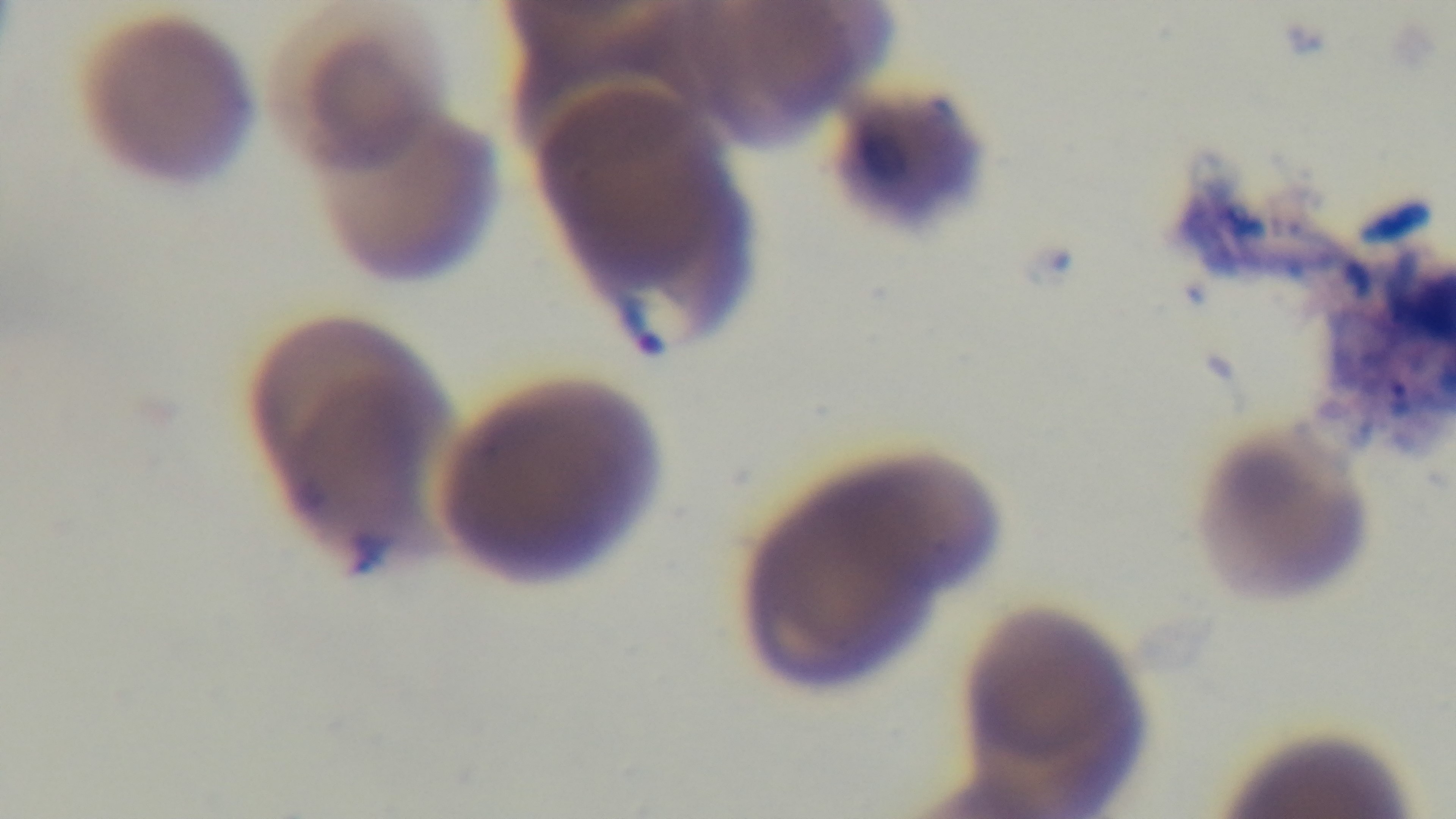

stain: Giemsa
field_of_view: one from the slide
modality: light microscopy
malaria_status: positive
objective: 100x oil immersion
capture: mounted 4K digital camera
preparation: thin smear